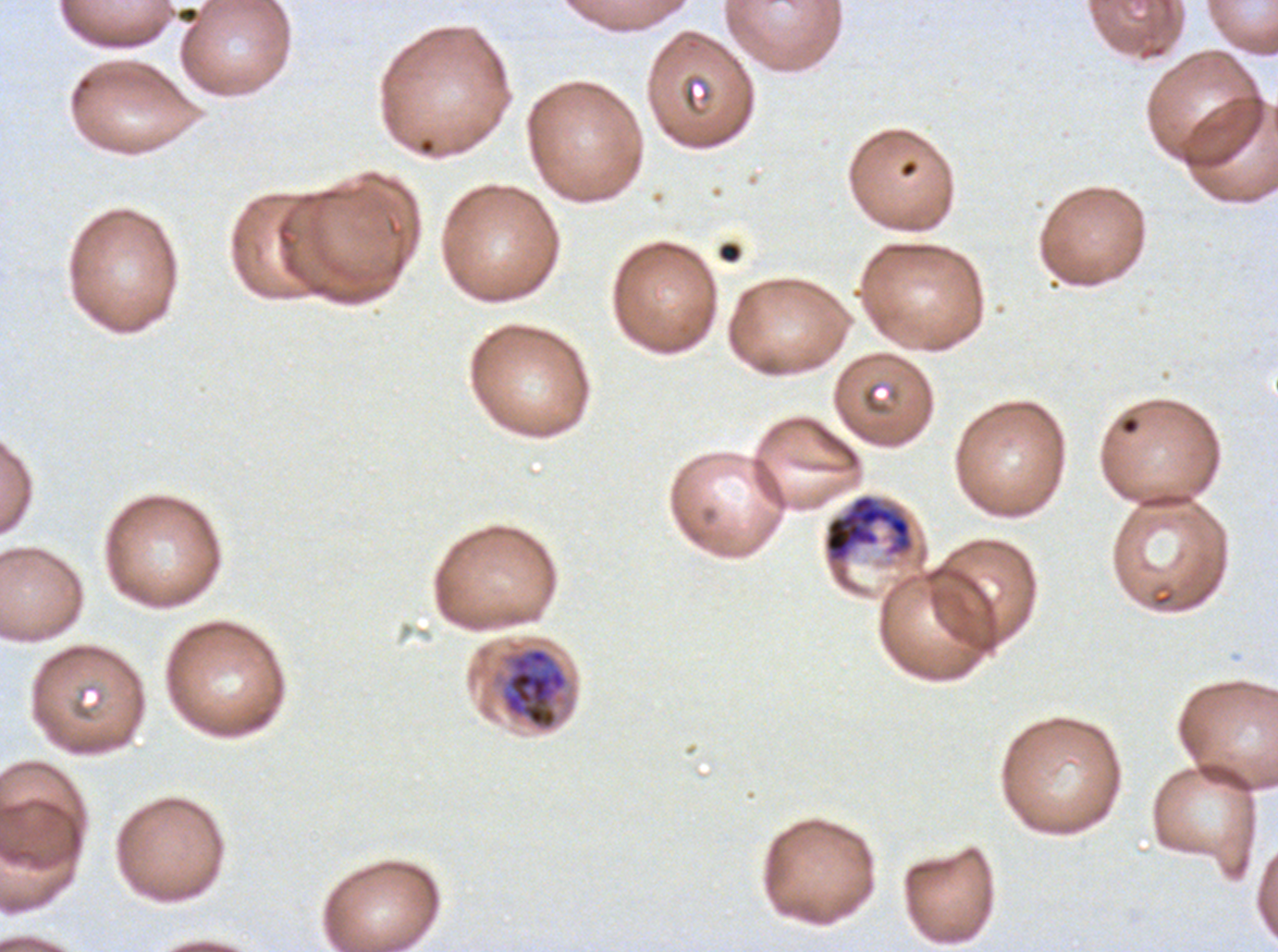

Approximate bounding boxes as {x1, y1, x2, y2} in pixels.
Summary:
  - Late trophozoite locations: {501, 647, 569, 730}
  - Early schizont locations: {823, 493, 915, 566}
  - Debris locations: {719, 242, 742, 263}
  - Preparation: thin blood smear
  - Image size: 1278×952 pixels
  - Stain: Giemsa
  - Field of view: one sub-image of a larger composite
  - Specimen: Plasmodium falciparum cultured ex vivo for 24 to 48 hours, from a patient in The Gambia
  - Life-cycle stages observed: late trophozoite, early schizont